Describe the morphology of the erythrocytes.
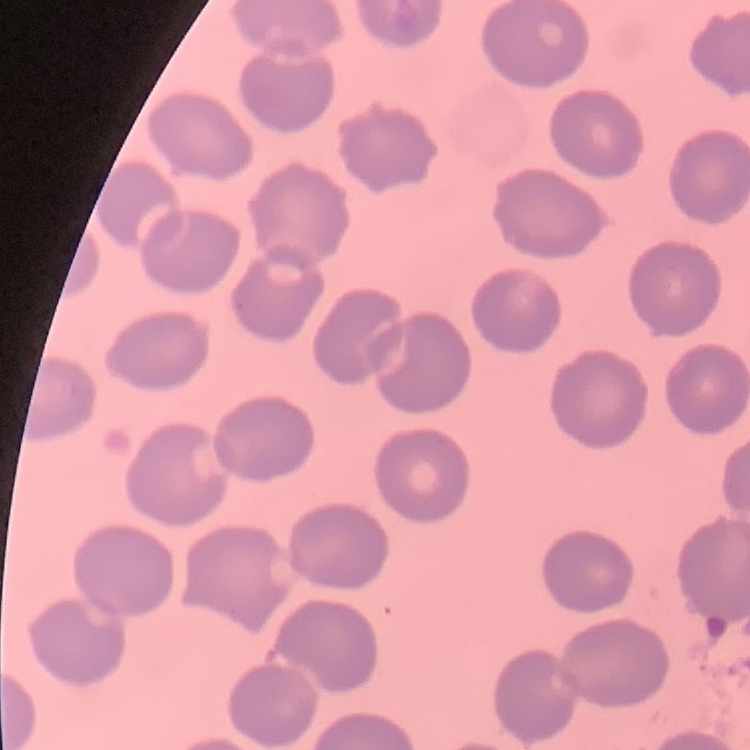

No rouleaux formation.

stain = Field's or Giemsa
image type = one tile cut from a larger photomicrograph
preparation = thin blood film